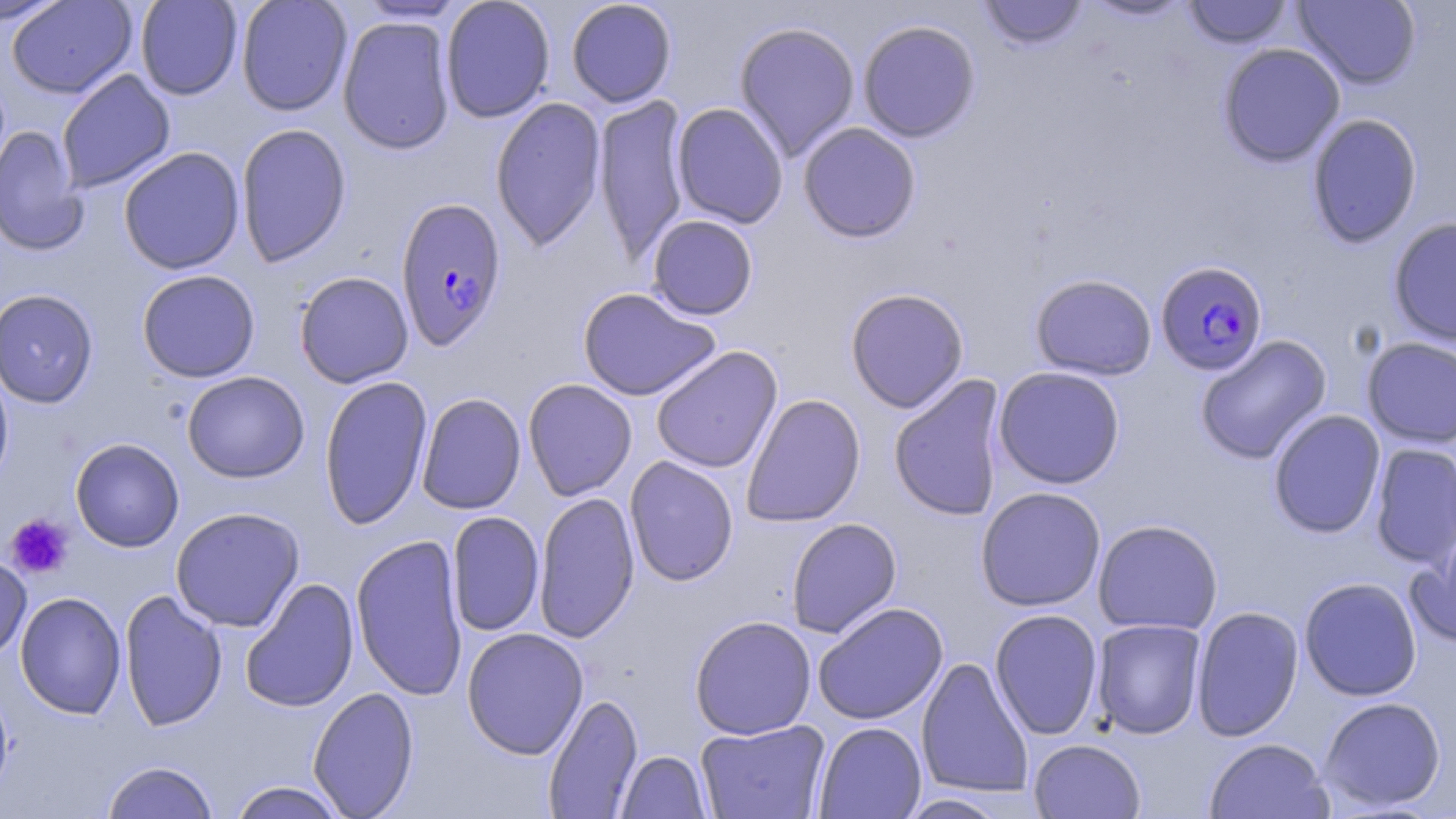

Approximate bounding boxes as [x1, y1, x2, y2] in pixels. Plasmodium falciparum-infected red blood cell locations: [395, 196, 508, 352], [1155, 260, 1268, 375]. Uninfected red blood cell locations: [0, 0, 71, 27], [7, 0, 137, 99], [135, 0, 243, 100], [236, 0, 353, 116], [440, 0, 556, 123], [566, 0, 677, 108], [1082, 0, 1194, 21], [1292, 0, 1421, 90], [353, 1, 469, 23], [978, 1, 1089, 51], [1183, 1, 1293, 49], [337, 16, 456, 155], [857, 19, 981, 143], [733, 21, 861, 161], [1218, 43, 1345, 167], [56, 69, 176, 193], [592, 95, 691, 263], [490, 97, 607, 252], [671, 102, 789, 229], [1307, 113, 1422, 248], [798, 122, 922, 243], [235, 123, 352, 267], [0, 125, 88, 256], [118, 147, 245, 274], [646, 215, 758, 320], [1388, 216, 1456, 347], [136, 269, 261, 382], [294, 271, 414, 388], [1030, 273, 1157, 381], [577, 287, 722, 401], [845, 287, 969, 413], [0, 288, 99, 409], [1195, 334, 1332, 465], [1361, 337, 1456, 448], [651, 345, 783, 474], [0, 362, 14, 491], [993, 366, 1125, 489], [182, 371, 309, 483], [888, 374, 1007, 521], [318, 375, 432, 530], [523, 378, 637, 500], [415, 392, 526, 515], [741, 393, 866, 528], [1268, 409, 1386, 538], [70, 437, 184, 552], [1370, 442, 1456, 568], [624, 455, 739, 587], [975, 486, 1106, 612], [533, 491, 640, 643], [170, 506, 305, 632], [447, 511, 545, 637], [786, 517, 902, 639], [1093, 519, 1223, 635], [351, 534, 468, 702], [1407, 537, 1456, 649], [0, 554, 32, 662], [240, 577, 360, 714], [1299, 577, 1422, 701], [119, 589, 227, 731], [15, 591, 126, 719], [812, 602, 948, 725], [1191, 605, 1304, 741], [989, 608, 1104, 740], [689, 615, 817, 740], [1092, 618, 1207, 739], [461, 627, 589, 760], [916, 656, 1033, 798], [0, 677, 15, 804], [307, 686, 420, 818], [543, 693, 643, 818], [1318, 696, 1446, 813], [696, 719, 830, 819], [814, 722, 926, 818], [1028, 738, 1146, 818], [1203, 738, 1333, 819], [617, 751, 711, 818], [101, 760, 219, 819], [228, 781, 349, 819], [897, 794, 1011, 818]. Platelet locations: [3, 514, 74, 580]. Slide-level diagnosis: Plasmodium falciparum. 1000x magnification. Light microscopy. One field of a larger specimen. Thin blood smear. Image is 1456×819 pixels. May-Grünwald-Giemsa-stained preparation.